Locate and identify every blood parasite.
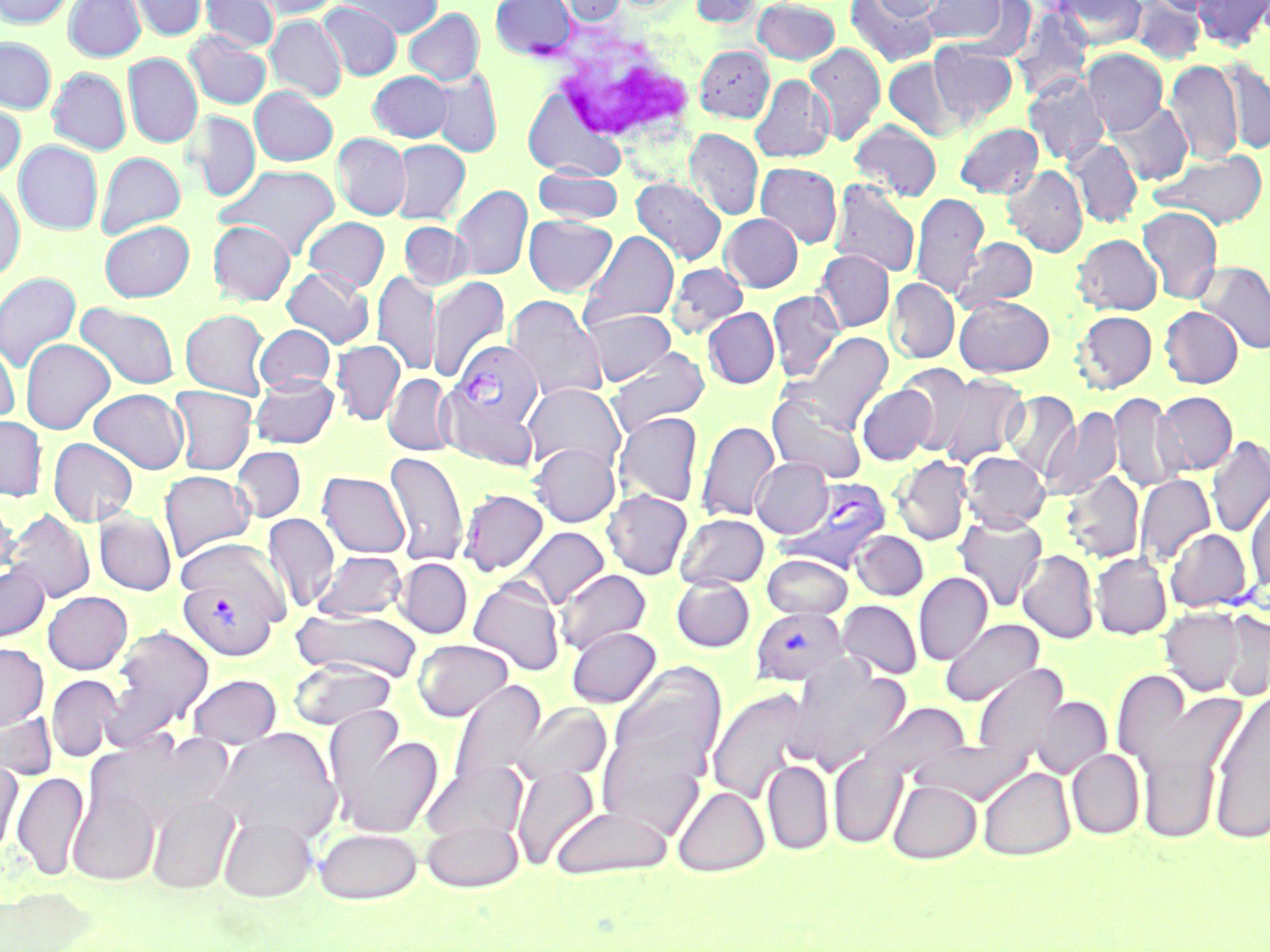
Approximate bounding boxes as (x1,y1)-(x2,y2) corner pairs in pixels.
Plasmodium vivax-infected red blood cells: (447,340)-(542,436), (782,477)-(892,571), (177,571)-(284,661), (750,606)-(850,686).
No Plasmodium falciparum, Plasmodium ovale, Plasmodium malariae, Babesia divergens, or Trypanosoma brucei observed.

slide-level diagnosis = Plasmodium vivax
modality = optical microscopy
magnification = 1000x
field of view = one of a larger specimen
white blood cell locations = approximate bounding boxes as (x1,y1)-(x2,y2) corner pairs in pixels: (551,29)-(695,148)
preparation = thin blood film
uninfected red blood cell locations = approximate bounding boxes as (x1,y1)-(x2,y2) corner pairs in pixels: (0,0)-(74,28), (63,0)-(145,61), (128,0)-(207,41), (200,0)-(279,52), (244,0)-(342,20), (336,0)-(443,37), (490,0)-(576,59), (551,0)-(628,26), (689,0)-(762,27), (753,0)-(839,65), (846,0)-(940,67), (871,0)-(949,20), (921,0)-(1009,45), (1054,0)-(1146,49), (1129,0)-(1205,64), (1147,0)-(1226,16), (1192,0)-(1270,50), (317,1)-(403,81), (954,1)-(1036,60), (1010,7)-(1094,101), (404,8)-(484,85), (265,15)-(347,102), (184,31)-(272,110), (0,37)-(56,114), (929,42)-(1018,125), (805,43)-(885,146), (695,45)-(774,122), (1081,48)-(1168,135), (123,53)-(202,148), (883,57)-(964,141), (1218,58)-(1270,155), (1165,60)-(1244,165), (47,67)-(131,155), (428,70)-(504,157), (367,71)-(453,142), (1023,74)-(1110,166), (749,75)-(834,163), (250,86)-(338,166), (522,86)-(627,182), (0,99)-(26,180), (1107,101)-(1193,185), (187,111)-(261,202), (849,119)-(942,201), (955,123)-(1043,198), (684,128)-(764,220), (332,133)-(411,220), (391,139)-(471,224), (1067,139)-(1143,228), (13,140)-(103,235), (1152,149)-(1268,229), (95,151)-(186,238), (755,162)-(842,248), (214,163)-(341,258), (1003,165)-(1087,257), (533,168)-(624,224), (631,178)-(727,266), (829,179)-(921,278), (0,181)-(25,280), (451,185)-(532,281), (910,192)-(988,299), (1137,206)-(1223,304), (720,213)-(803,292), (523,214)-(617,296), (303,216)-(390,291), (99,220)-(194,302), (207,221)-(295,305), (399,221)-(472,290), (581,230)-(679,328), (1072,234)-(1162,315), (952,236)-(1038,313), (814,250)-(894,333), (1197,261)-(1270,355), (666,262)-(749,339), (281,266)-(374,348), (373,270)-(440,376), (0,272)-(81,374), (426,276)-(510,381), (885,278)-(960,364), (767,289)-(844,380), (505,295)-(607,401), (954,295)-(1054,376), (75,302)-(180,390), (1159,306)-(1243,388), (581,307)-(675,385), (703,307)-(780,389), (180,308)-(271,399), (1074,310)-(1157,393), (254,324)-(335,393), (789,331)-(893,432), (20,338)-(115,434), (0,340)-(19,425), (331,340)-(405,426), (605,348)-(710,439), (897,364)-(979,457), (933,372)-(1028,467), (384,373)-(455,456), (250,374)-(339,449), (522,382)-(625,473), (857,383)-(938,466), (169,386)-(257,475), (89,388)-(190,474), (440,389)-(538,472), (767,391)-(867,483), (1002,391)-(1081,480), (1109,392)-(1184,492), (1154,392)-(1237,475), (1041,406)-(1122,502), (613,412)-(703,507), (0,415)-(48,501), (696,420)-(780,522), (1206,435)-(1270,538), (48,438)-(139,527), (529,442)-(620,527), (232,446)-(306,522), (385,450)-(469,567), (962,452)-(1050,531), (891,455)-(972,545), (751,457)-(833,537), (158,470)-(255,561), (1061,470)-(1144,563), (318,471)-(409,558), (1135,473)-(1215,567), (459,488)-(549,576), (602,489)-(692,580), (1246,490)-(1270,594), (0,493)-(18,581), (4,508)-(96,602), (94,509)-(176,595), (262,513)-(339,613), (675,513)-(769,589), (953,513)-(1048,611), (516,526)-(609,608), (1166,529)-(1253,612), (851,531)-(928,601), (174,537)-(289,627), (312,550)-(407,621), (1017,550)-(1099,644), (762,553)-(853,619), (1091,553)-(1172,639), (395,558)-(473,638), (0,562)-(50,643), (555,569)-(651,655), (913,572)-(993,665), (670,576)-(755,652), (468,577)-(565,676), (43,591)-(132,674), (837,600)-(922,679), (1160,607)-(1245,695), (291,609)-(423,683), (1218,610)-(1270,700), (941,618)-(1045,707), (106,624)-(214,739), (566,626)-(661,707), (413,638)-(513,722), (0,643)-(49,731), (288,660)-(397,731), (608,660)-(728,794), (788,660)-(910,774), (973,664)-(1068,757), (1111,669)-(1194,774), (46,674)-(122,763), (187,674)-(282,748), (448,678)-(546,793), (706,688)-(818,805), (1206,690)-(1270,844), (1030,697)-(1112,778), (511,702)-(611,787), (865,702)-(973,783), (594,709)-(718,841), (0,711)-(57,780), (324,714)-(444,840), (1133,727)-(1229,845), (211,728)-(342,844), (91,732)-(236,836), (911,742)-(1036,804), (1067,749)-(1145,839), (828,750)-(907,849), (762,759)-(833,854), (421,760)-(528,845), (0,761)-(23,859), (510,764)-(600,870), (978,767)-(1076,860), (11,770)-(89,881), (67,780)-(162,885), (888,780)-(982,864), (672,785)-(769,877), (145,792)-(240,895), (549,806)-(673,880), (218,813)-(317,902), (420,817)-(526,893), (313,827)-(423,904), (0,887)-(100,951)
image size = 1270×952 pixels
stain = May-Grünwald-Giemsa